Classify this cell by malaria status.
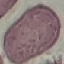
Uninfected.

Thin blood smear. Photographed with a smartphone camera at the microscope eyepiece. Automatically extracted cell patch, resized to 64 × 64 pixels. Giemsa-stained preparation.